Describe the morphology of the erythrocytes.
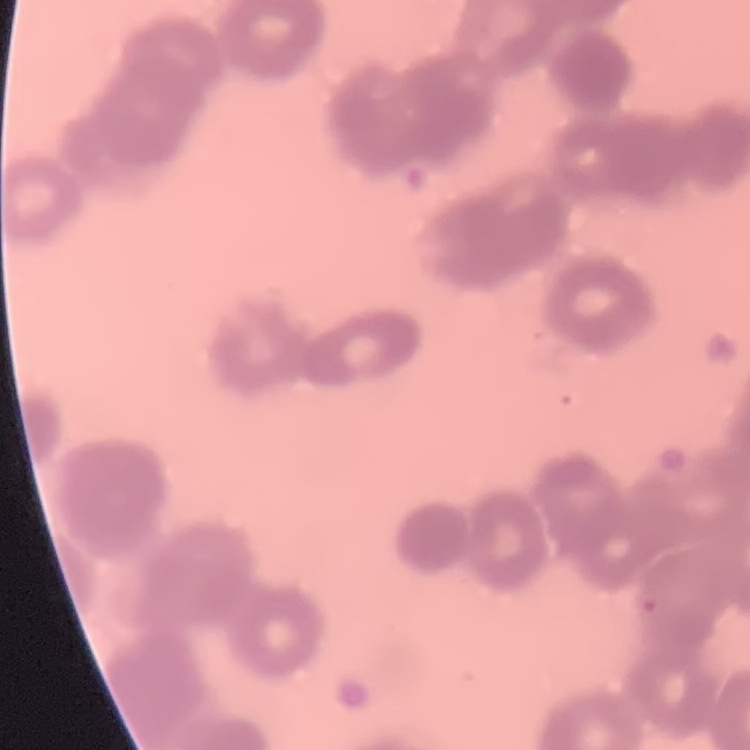
Rouleaux formation.

Summary:
  - Stain: Field's or Giemsa
  - Image type: square crop of a larger photomicrograph
  - Preparation: thin blood film